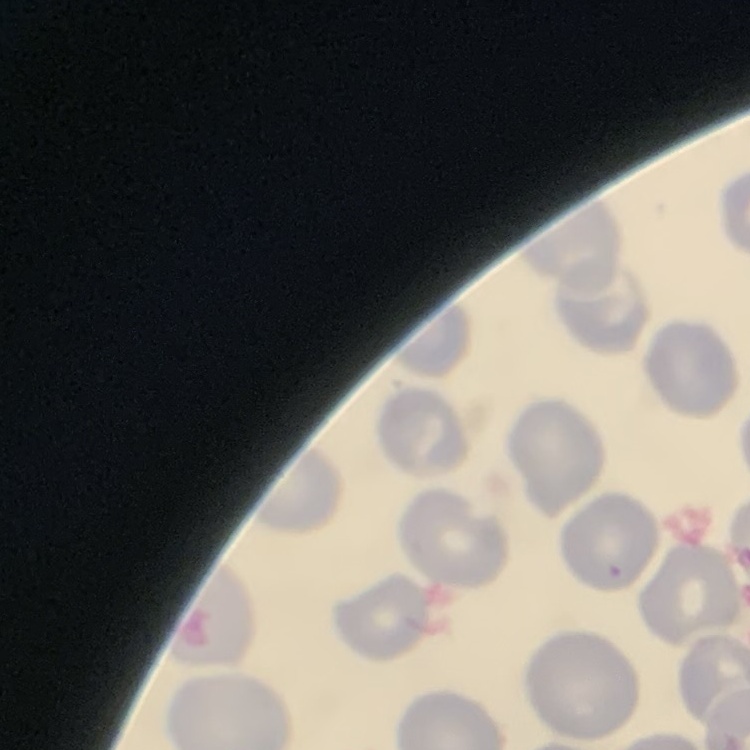 The erythrocytes show no rouleaux formation. Thin blood film. Field's or Giemsa stain. Square crop of a larger photomicrograph.